Describe the morphology of the erythrocytes.
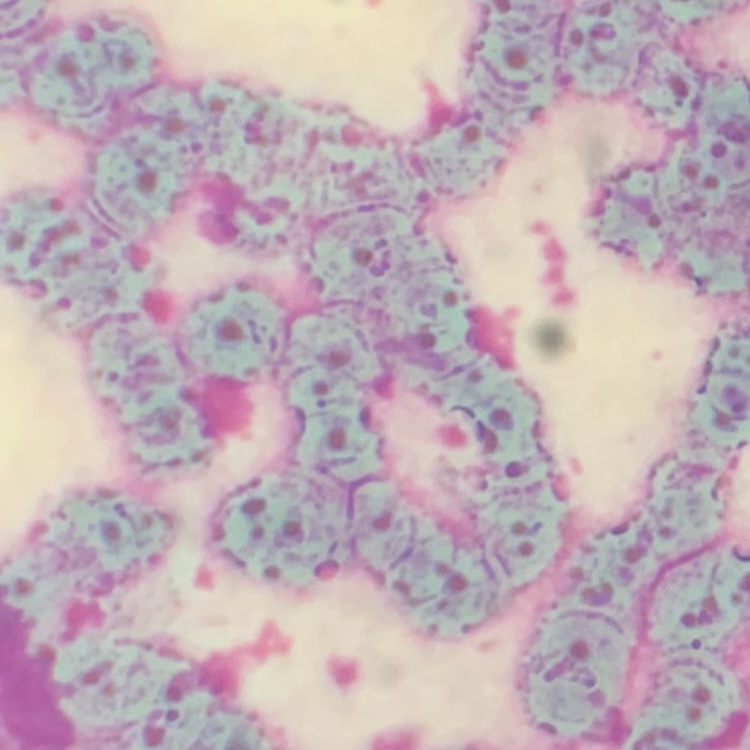
They show rouleaux formation.

Summary:
  - Image type: one tile cut from a larger photomicrograph
  - Stain: Field's or Giemsa
  - Preparation: thin blood film